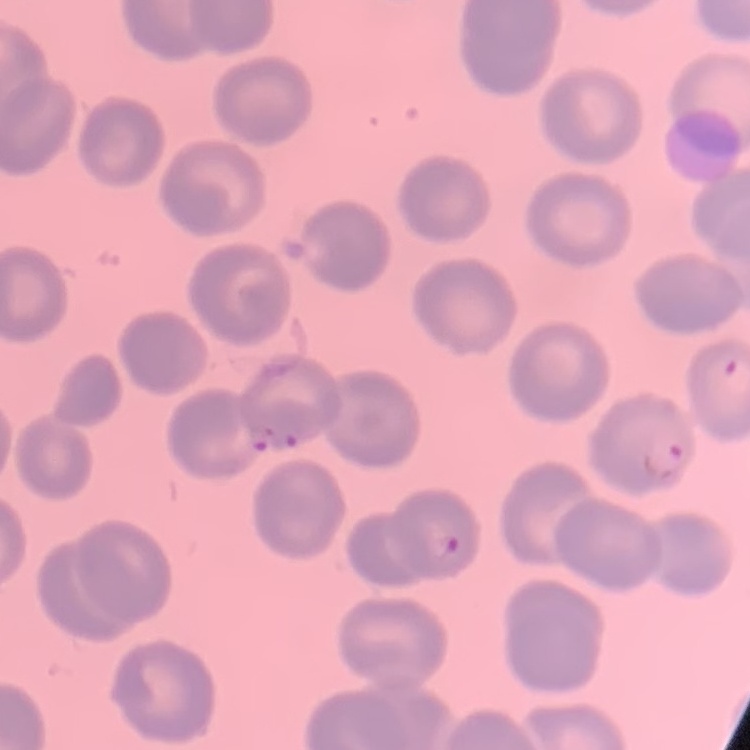
Summary:
  - Red blood cell morphology: no rouleaux formation
  - Preparation: thin blood smear
  - Image type: square crop of a larger photomicrograph
  - Stain: Field's or Giemsa